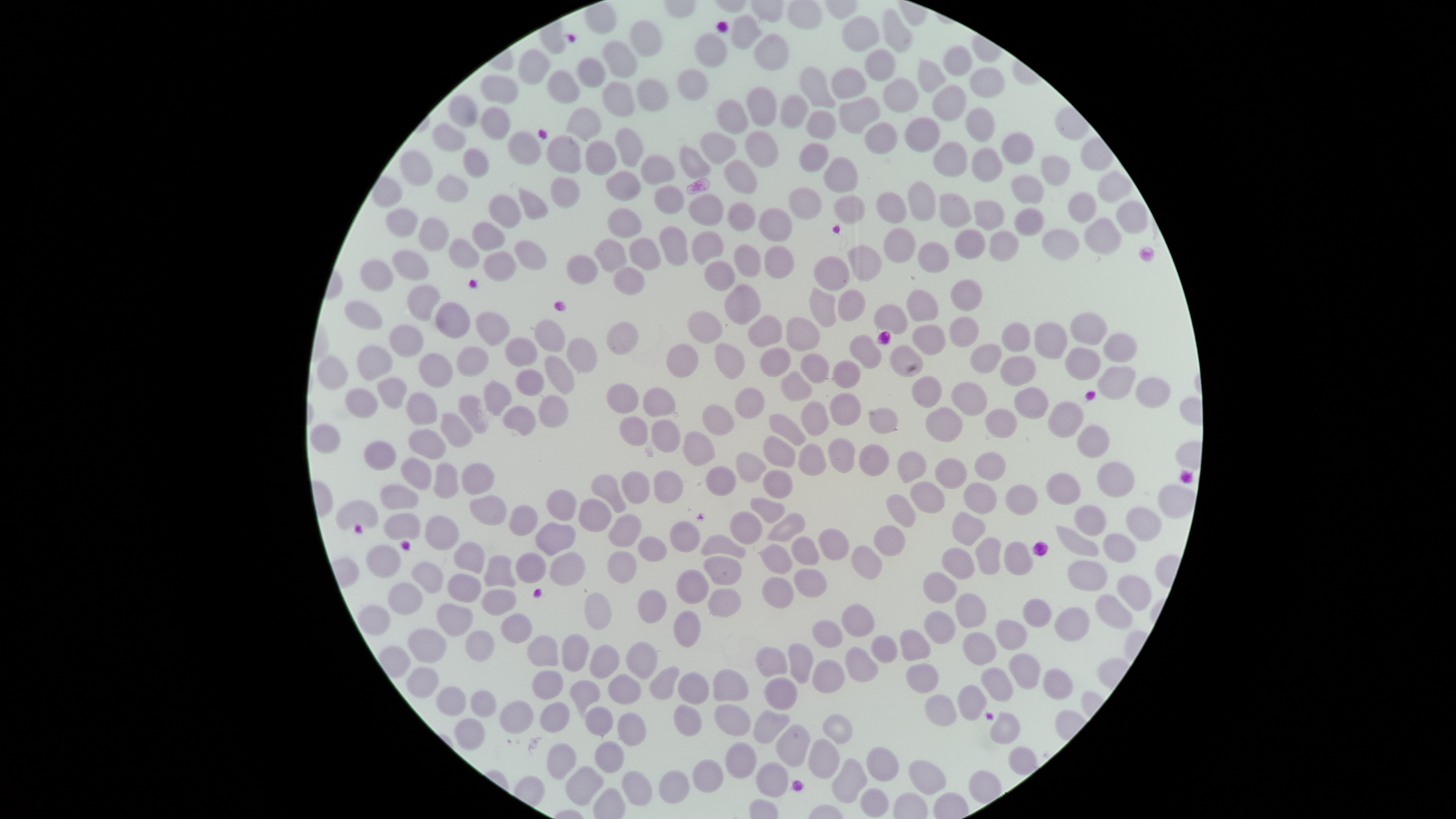

image size = 1456×819 pixels
presence = no malaria parasites detected
stain = Giemsa
capture = smartphone photograph through the microscope eyepiece
uninfected red blood cells = approximate bounding boxes as {left, top, right, bottom} in pixels: {883, 9, 913, 53}, {730, 14, 763, 50}, {841, 16, 879, 53}, {630, 21, 661, 56}, {694, 33, 726, 69}, {754, 34, 789, 71}, {603, 41, 637, 78}, {943, 45, 973, 77}, {518, 48, 550, 84}, {864, 49, 895, 81}, {576, 57, 604, 88}, {917, 59, 947, 94}, {799, 66, 836, 109}, {831, 68, 867, 99}, {969, 68, 1004, 99}, {678, 69, 709, 101}, {547, 71, 580, 104}, {480, 75, 518, 104}, {883, 77, 919, 114}, {636, 78, 668, 112}, {601, 81, 636, 117}, {931, 85, 966, 122}, {747, 87, 777, 126}, {780, 94, 807, 128}, {448, 95, 476, 129}, {839, 97, 880, 134}, {717, 100, 749, 135}, {480, 106, 510, 141}, {566, 107, 602, 142}, {966, 107, 994, 142}, {806, 110, 836, 138}, {904, 117, 939, 152}, {864, 122, 898, 154}, {432, 123, 466, 152}, {614, 128, 643, 168}, {745, 130, 779, 168}, {508, 131, 542, 166}, {699, 131, 736, 166}, {1002, 132, 1033, 165}, {548, 137, 582, 174}, {585, 140, 617, 175}, {798, 142, 829, 172}, {933, 142, 968, 176}, {680, 145, 711, 179}, {972, 147, 1004, 182}, {463, 148, 488, 177}, {400, 151, 433, 186}, {640, 155, 675, 185}, {822, 156, 858, 193}, {1041, 156, 1071, 186}, {723, 158, 758, 193}, {605, 170, 641, 202}, {1098, 170, 1134, 204}, {436, 174, 469, 202}, {1010, 175, 1045, 205}, {549, 177, 580, 208}, {907, 180, 936, 222}, {654, 185, 684, 215}, {788, 186, 823, 220}, {517, 188, 548, 220}, {875, 191, 908, 224}, {1067, 191, 1097, 225}, {833, 193, 866, 225}, {489, 194, 523, 230}, {689, 194, 724, 226}, {939, 194, 971, 227}, {974, 200, 1004, 231}, {1116, 200, 1147, 234}, {727, 201, 756, 231}, {607, 207, 641, 239}, {758, 207, 793, 242}, {1013, 207, 1045, 237}, {386, 209, 417, 237}, {417, 217, 449, 252}, {1085, 218, 1122, 255}, {472, 220, 506, 252}, {658, 226, 689, 267}, {882, 226, 917, 264}, {954, 227, 986, 259}, {1041, 228, 1081, 262}, {988, 229, 1020, 262}, {691, 231, 725, 265}, {629, 237, 661, 271}, {448, 239, 479, 269}, {514, 239, 546, 271}, {595, 239, 627, 275}, {917, 240, 951, 273}, {732, 243, 761, 278}, {846, 244, 883, 282}, {764, 245, 794, 279}, {391, 249, 429, 282}, {483, 251, 517, 283}, {812, 255, 851, 291}, {566, 256, 598, 284}, {359, 259, 394, 292}, {704, 262, 734, 291}, {613, 267, 645, 295}, {950, 279, 983, 312}, {406, 284, 441, 322}, {724, 284, 760, 326}, {809, 286, 837, 329}, {837, 288, 866, 322}, {906, 288, 940, 323}, {344, 301, 382, 331}, {873, 302, 909, 334}, {435, 303, 470, 339}, {686, 310, 723, 345}, {476, 313, 509, 346}, {1070, 313, 1106, 344}, {747, 314, 783, 348}, {785, 315, 822, 352}, {949, 316, 980, 347}, {535, 320, 564, 353}, {606, 322, 639, 355}, {1001, 322, 1029, 353}, {1033, 322, 1067, 360}, {911, 324, 947, 356}, {389, 325, 424, 358}, {848, 334, 883, 370}, {1103, 334, 1136, 363}, {504, 337, 539, 367}, {566, 337, 599, 373}, {714, 341, 746, 380}, {666, 342, 700, 378}, {889, 344, 924, 376}, {970, 344, 1004, 376}, {357, 346, 392, 382}, {758, 346, 793, 377}, {457, 347, 489, 377}, {1065, 348, 1101, 380}, {799, 352, 830, 384}, {419, 353, 454, 388}, {544, 355, 576, 395}, {317, 356, 348, 390}, {1000, 357, 1036, 387}, {832, 359, 862, 389}, {1098, 366, 1137, 400}, {515, 368, 545, 396}, {780, 369, 813, 402}, {910, 376, 942, 408}, {377, 377, 408, 409}, {1135, 377, 1171, 408}, {482, 379, 513, 417}, {951, 383, 986, 415}, {607, 384, 638, 413}, {1015, 386, 1050, 419}, {643, 387, 676, 418}, {344, 389, 379, 419}, {735, 389, 765, 419}, {405, 391, 438, 426}, {829, 392, 862, 426}, {537, 394, 570, 428}, {457, 395, 489, 434}, {799, 400, 831, 437}, {1047, 402, 1085, 439}, {502, 405, 537, 436}, {703, 405, 733, 435}, {868, 407, 899, 435}, {926, 408, 962, 442}, {984, 409, 1017, 439}, {439, 410, 473, 449}, {769, 414, 806, 447}, {619, 416, 648, 446}, {651, 419, 680, 452}, {310, 424, 341, 454}, {1076, 425, 1110, 458}, {407, 429, 447, 461}, {683, 432, 715, 466}, {762, 434, 796, 468}, {826, 437, 857, 474}, {363, 440, 396, 471}, {798, 443, 827, 476}, {858, 443, 890, 477}, {734, 451, 767, 482}, {897, 452, 927, 483}, {974, 452, 1006, 482}, {400, 457, 432, 491}, {935, 458, 966, 489}, {432, 461, 459, 499}, {460, 461, 496, 495}, {1096, 462, 1134, 498}, {705, 465, 736, 497}, {762, 469, 794, 499}, {653, 470, 683, 504}, {621, 472, 649, 504}, {1046, 473, 1079, 505}, {590, 475, 626, 513}, {911, 482, 944, 513}, {963, 482, 997, 515}, {379, 484, 419, 511}, {1005, 485, 1038, 516}, {1158, 485, 1195, 518}, {546, 488, 577, 521}, {468, 494, 508, 526}, {888, 495, 916, 527}, {578, 497, 613, 532}, {749, 497, 786, 525}, {334, 499, 379, 530}, {506, 504, 538, 537}, {1073, 505, 1107, 537}, {1125, 506, 1162, 541}, {728, 510, 763, 545}, {765, 512, 807, 542}, {952, 512, 987, 546}, {382, 513, 421, 541}, {607, 513, 642, 547}, {424, 515, 460, 552}, {668, 519, 701, 553}, {534, 521, 576, 557}, {875, 525, 905, 557}, {1056, 526, 1100, 557}, {817, 527, 850, 560}, {1103, 533, 1136, 563}, {700, 534, 746, 559}, {637, 535, 669, 562}, {790, 535, 821, 565}, {976, 537, 1000, 575}, {453, 541, 486, 575}, {1003, 541, 1033, 575}, {756, 542, 793, 575}, {365, 544, 402, 579}, {851, 545, 882, 580}, {942, 548, 975, 580}, {606, 550, 638, 584}, {515, 551, 547, 584}, {549, 552, 586, 587}, {483, 554, 516, 588}, {702, 556, 742, 585}, {1067, 559, 1108, 592}, {410, 560, 445, 595}, {793, 567, 828, 598}, {676, 568, 710, 604}, {922, 572, 957, 603}, {446, 573, 482, 604}, {1116, 575, 1151, 610}, {761, 576, 794, 609}, {387, 581, 424, 615}, {707, 587, 742, 617}, {637, 588, 667, 624}, {481, 589, 516, 616}, {582, 591, 612, 630}, {953, 593, 986, 629}, {1095, 594, 1133, 629}, {1023, 598, 1052, 628}, {436, 602, 474, 637}, {842, 604, 875, 637}, {1054, 607, 1090, 642}, {672, 609, 701, 648}, {925, 610, 954, 643}, {500, 613, 533, 643}, {811, 620, 843, 650}, {996, 620, 1027, 650}, {406, 628, 447, 662}, {465, 629, 495, 662}, {900, 630, 931, 662}, {962, 631, 998, 666}, {561, 632, 590, 673}, {527, 634, 559, 667}, {870, 635, 898, 665}, {625, 641, 659, 679}, {787, 642, 815, 684}, {589, 643, 620, 680}, {844, 645, 879, 683}, {755, 647, 788, 678}, {1007, 652, 1043, 690}, {812, 660, 845, 693}, {905, 662, 940, 694}, {648, 665, 680, 700}, {406, 666, 440, 699}, {980, 666, 1014, 702}, {1042, 667, 1074, 700}, {531, 669, 564, 699}, {713, 669, 750, 702}, {678, 672, 710, 704}, {607, 673, 643, 704}, {764, 676, 799, 711}, {567, 679, 602, 722}, {957, 684, 988, 721}, {435, 686, 467, 717}, {470, 689, 497, 718}, {923, 693, 958, 727}, {499, 700, 535, 735}, {539, 701, 570, 733}, {673, 703, 703, 737}, {714, 703, 752, 736}, {584, 705, 614, 737}, {753, 709, 791, 744}, {989, 710, 1021, 745}, {616, 712, 647, 746}, {821, 714, 853, 744}, {454, 717, 486, 751}, {774, 724, 811, 768}, {808, 737, 841, 779}, {594, 740, 626, 774}, {724, 741, 757, 779}, {546, 742, 577, 781}, {1008, 745, 1038, 776}, {866, 746, 901, 782}, {830, 757, 868, 804}, {691, 759, 725, 793}, {908, 759, 948, 796}, {756, 761, 790, 798}, {564, 764, 605, 806}, {658, 769, 690, 804}, {622, 771, 654, 806}, {860, 787, 890, 818}
field of view = single
preparation = thin smear of blood
visible region = circular